Give the position of every Plasmodium parasite.
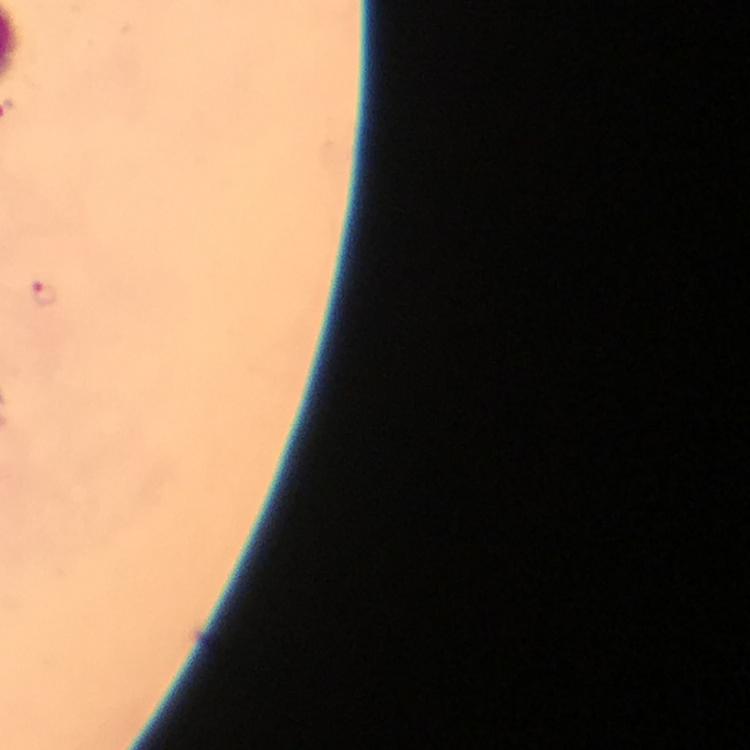
Approximate object centers, in pixels from the top-left corner.
Plasmodium parasites: (x=43, y=294).

capture = smartphone camera through the microscope
image size = 750×750 pixels
preparation = thick blood smear
magnification = 100x
context = from a malaria diagnostic workup
stain = Giemsa
immersion oil = applied
cropped from = a single field of view